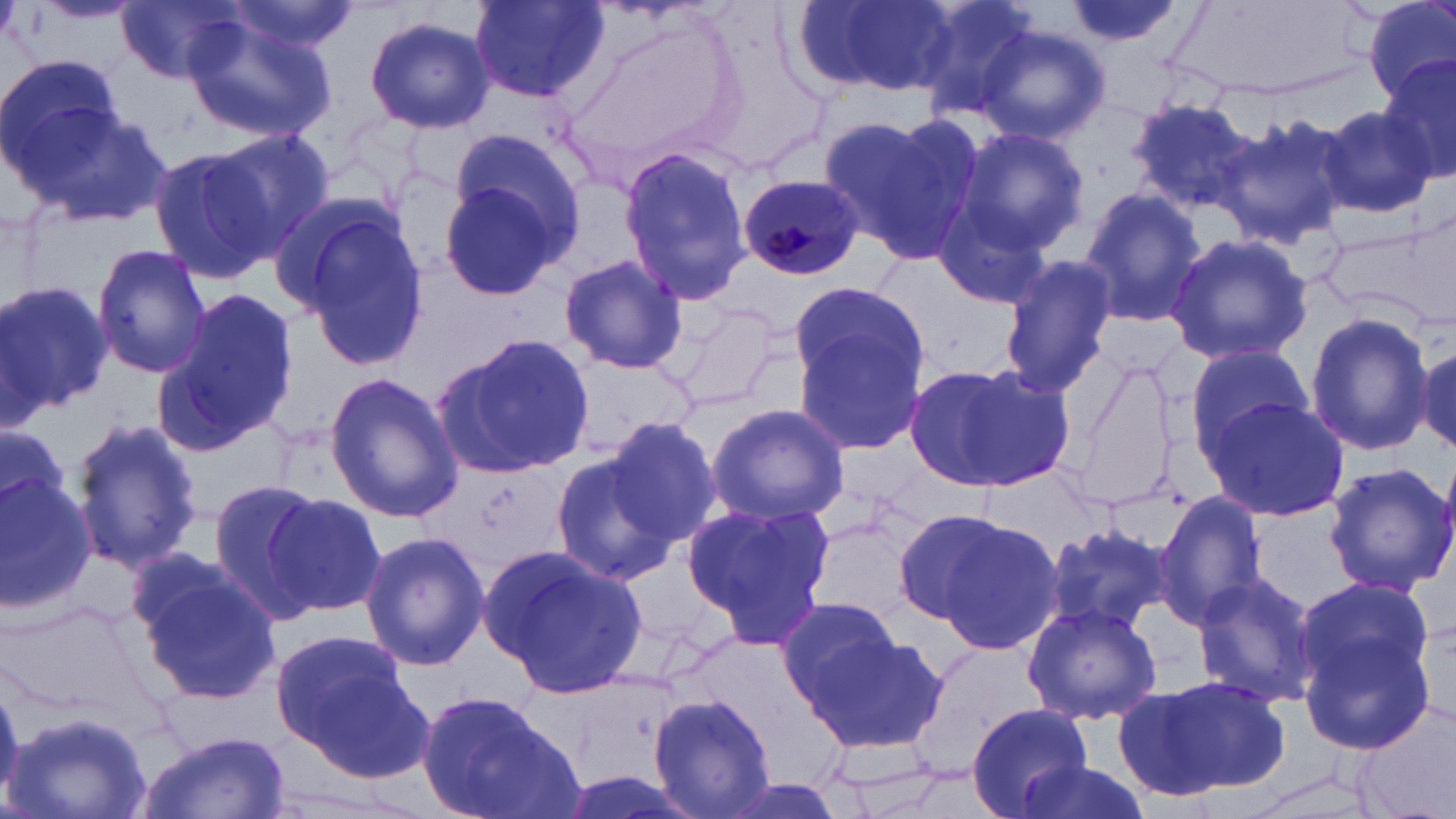

Plasmodium malariae-infected red blood cell locations = approximate bounding boxes as named x1/y1/x2/y2 corners in pixels: (x1=735, y1=175, x2=864, y2=281)
slide-level diagnosis = Plasmodium malariae
image size = 1456×819 pixels
uninfected red blood cell locations = approximate bounding boxes as named x1/y1/x2/y2 corners in pixels: (x1=117, y1=0, x2=248, y2=84), (x1=470, y1=0, x2=608, y2=103), (x1=800, y1=0, x2=958, y2=98), (x1=907, y1=0, x2=1039, y2=120), (x1=1056, y1=0, x2=1185, y2=57), (x1=1362, y1=0, x2=1455, y2=103), (x1=220, y1=1, x2=360, y2=58), (x1=181, y1=12, x2=338, y2=140), (x1=364, y1=14, x2=495, y2=133), (x1=976, y1=25, x2=1109, y2=147), (x1=1, y1=54, x2=126, y2=184), (x1=1377, y1=56, x2=1455, y2=181), (x1=21, y1=98, x2=173, y2=232), (x1=1128, y1=98, x2=1260, y2=213), (x1=1316, y1=104, x2=1438, y2=219), (x1=821, y1=111, x2=982, y2=265), (x1=1217, y1=113, x2=1355, y2=248), (x1=957, y1=126, x2=1089, y2=253), (x1=208, y1=129, x2=335, y2=251), (x1=439, y1=145, x2=584, y2=303), (x1=617, y1=146, x2=756, y2=310), (x1=148, y1=147, x2=278, y2=283), (x1=930, y1=189, x2=1062, y2=315), (x1=1077, y1=189, x2=1208, y2=325), (x1=281, y1=200, x2=430, y2=368), (x1=1319, y1=220, x2=1445, y2=324), (x1=1163, y1=231, x2=1316, y2=367), (x1=92, y1=244, x2=212, y2=377), (x1=998, y1=250, x2=1119, y2=400), (x1=557, y1=254, x2=690, y2=376), (x1=0, y1=280, x2=112, y2=417), (x1=790, y1=282, x2=927, y2=394), (x1=154, y1=285, x2=302, y2=455), (x1=1304, y1=310, x2=1433, y2=457), (x1=791, y1=320, x2=930, y2=460), (x1=436, y1=334, x2=597, y2=476), (x1=1188, y1=342, x2=1312, y2=454), (x1=1415, y1=343, x2=1456, y2=452), (x1=906, y1=362, x2=1072, y2=493), (x1=324, y1=370, x2=462, y2=524), (x1=1203, y1=396, x2=1352, y2=522), (x1=704, y1=403, x2=848, y2=525), (x1=68, y1=414, x2=205, y2=573), (x1=603, y1=416, x2=723, y2=542), (x1=1, y1=421, x2=68, y2=516), (x1=548, y1=450, x2=677, y2=583), (x1=1324, y1=462, x2=1455, y2=595), (x1=0, y1=468, x2=99, y2=613), (x1=206, y1=477, x2=332, y2=619), (x1=260, y1=489, x2=387, y2=623), (x1=1155, y1=490, x2=1268, y2=626), (x1=682, y1=501, x2=833, y2=643), (x1=900, y1=508, x2=1061, y2=653), (x1=1041, y1=517, x2=1175, y2=638), (x1=359, y1=530, x2=489, y2=671), (x1=487, y1=543, x2=645, y2=698), (x1=138, y1=566, x2=285, y2=707), (x1=1190, y1=571, x2=1322, y2=710), (x1=1292, y1=584, x2=1439, y2=755), (x1=777, y1=594, x2=905, y2=714), (x1=1020, y1=602, x2=1164, y2=724), (x1=269, y1=627, x2=419, y2=765), (x1=800, y1=631, x2=949, y2=755), (x1=1112, y1=674, x2=1293, y2=800), (x1=649, y1=688, x2=782, y2=819), (x1=417, y1=692, x2=575, y2=819), (x1=965, y1=703, x2=1092, y2=819), (x1=2, y1=709, x2=154, y2=819), (x1=135, y1=731, x2=293, y2=819), (x1=1009, y1=758, x2=1151, y2=819)
modality = light microscopy
preparation = thin blood film
magnification = 1000x
stain = May-Grünwald-Giemsa
field of view = single